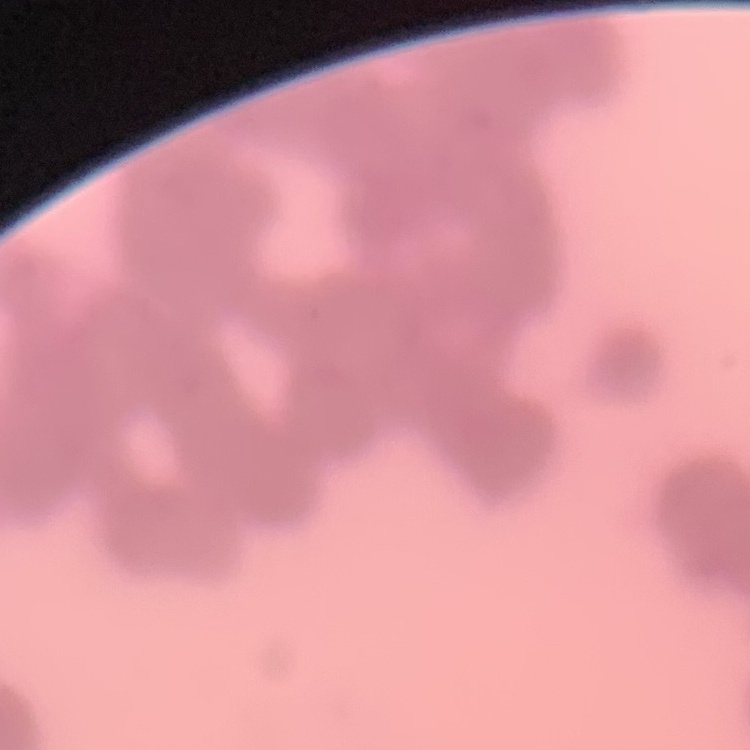

Summary:
  - Red blood cell morphology: rouleaux formation
  - Stain: Field's or Giemsa
  - Preparation: thin peripheral smear
  - Image type: one tile cut from a larger photomicrograph